Name the parasite shown.
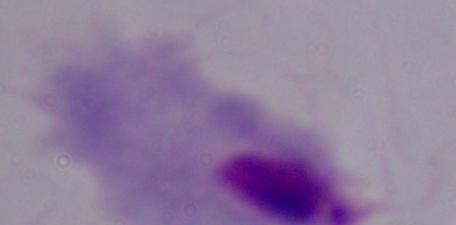

This is a trichomonad.

Summary:
  - Magnification: 1000x
  - Modality: micrograph